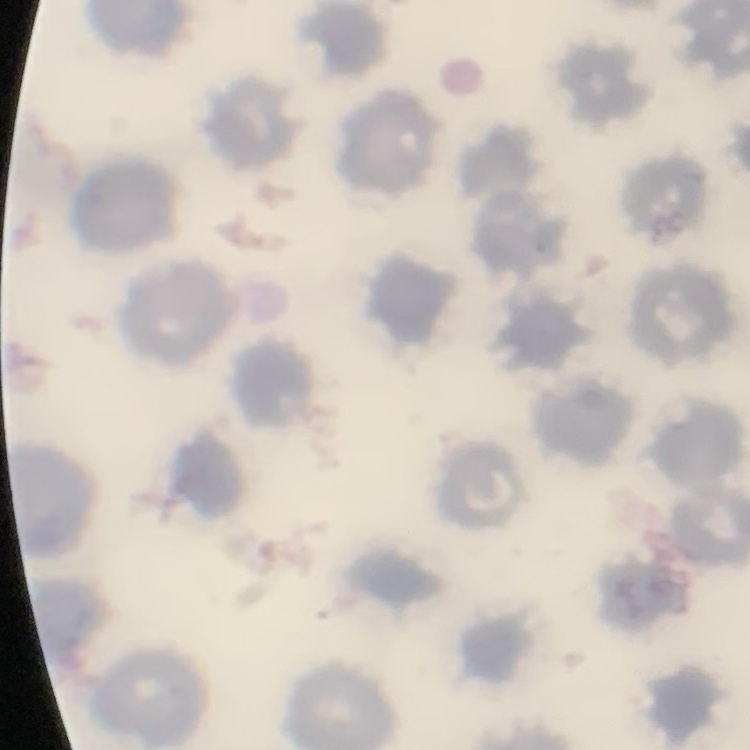 The erythrocytes show no rouleaux formation. Field's or Giemsa stain. Square crop of a larger photomicrograph. Thin blood film.